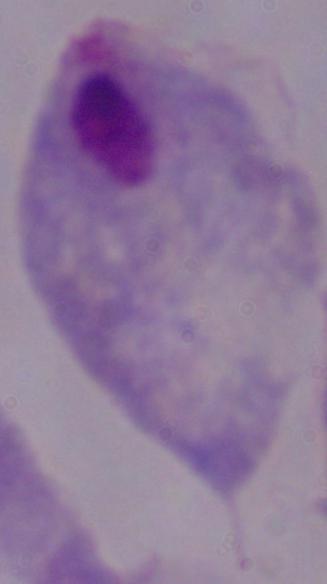

{
  "identification": "trichomonad",
  "modality": "photomicrograph",
  "magnification": "1000x"
}